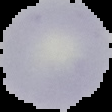
Image is 112×112 pixels. Segmented cell region on a black background. From a thin blood film. Malaria status: uninfected.